Assess this cell for malaria.
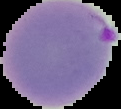
Parasitized.

Summary:
  - Image type: segmented cell region on a black background
  - Image size: 121×109 pixels
  - Preparation: thin blood smear